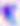
Summary:
  - Magnification: 400x
  - Modality: micrograph
  - Identification: Toxoplasma gondii